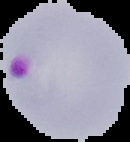

Cell region segmented out of the field of view; the surrounding area is masked to black. Result: Plasmodium parasites detected. From a thin blood smear. Image is 130×142 pixels.